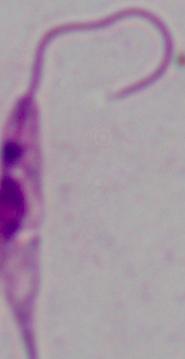
A Leishmania parasite is shown. Photomicrograph. 1000x magnification.